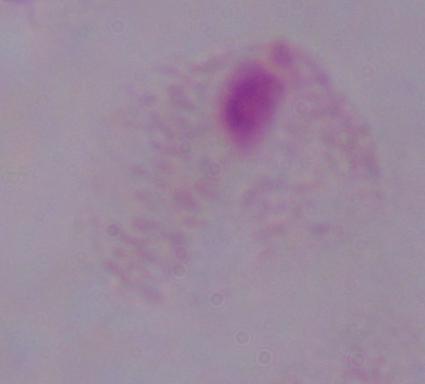

Photomicrograph. 1000x magnification. A trichomonad is shown.